Locate every Plasmodium falciparum-infected red blood cell.
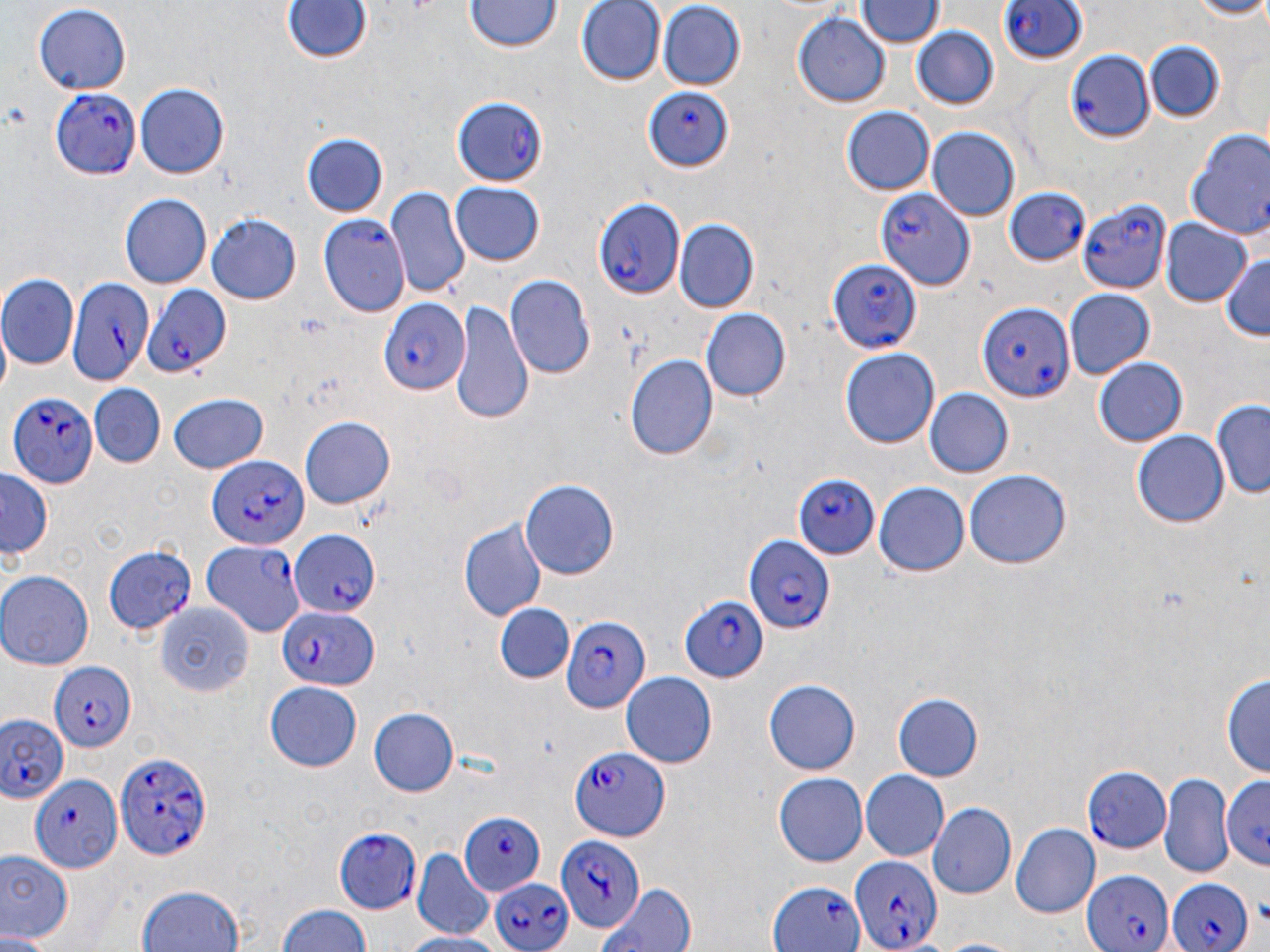

Approximate bounding boxes as named x1/y1/x2/y2 corners in pixels.
Plasmodium falciparum-infected red blood cells: (x1=994, y1=0, x2=1092, y2=75), (x1=1063, y1=48, x2=1151, y2=143), (x1=49, y1=86, x2=142, y2=179), (x1=644, y1=86, x2=734, y2=171), (x1=450, y1=96, x2=551, y2=184), (x1=874, y1=178, x2=977, y2=301), (x1=1003, y1=187, x2=1090, y2=273), (x1=593, y1=195, x2=687, y2=298), (x1=1077, y1=198, x2=1171, y2=295), (x1=319, y1=212, x2=411, y2=318), (x1=828, y1=259, x2=922, y2=353), (x1=65, y1=277, x2=149, y2=386), (x1=139, y1=282, x2=231, y2=378), (x1=378, y1=297, x2=469, y2=397), (x1=978, y1=299, x2=1075, y2=403), (x1=9, y1=393, x2=98, y2=490), (x1=208, y1=458, x2=307, y2=551), (x1=790, y1=475, x2=879, y2=560), (x1=289, y1=530, x2=381, y2=615), (x1=744, y1=534, x2=832, y2=634), (x1=202, y1=539, x2=304, y2=639), (x1=103, y1=547, x2=196, y2=637), (x1=677, y1=596, x2=769, y2=684), (x1=274, y1=608, x2=377, y2=691), (x1=560, y1=612, x2=654, y2=711), (x1=48, y1=663, x2=135, y2=752), (x1=0, y1=712, x2=70, y2=806), (x1=568, y1=744, x2=670, y2=841), (x1=115, y1=751, x2=211, y2=862), (x1=1084, y1=766, x2=1171, y2=854), (x1=28, y1=775, x2=120, y2=872), (x1=457, y1=811, x2=545, y2=896), (x1=334, y1=825, x2=423, y2=914), (x1=555, y1=835, x2=642, y2=934), (x1=848, y1=853, x2=942, y2=951), (x1=1081, y1=870, x2=1172, y2=952), (x1=488, y1=875, x2=574, y2=952), (x1=1164, y1=876, x2=1255, y2=952), (x1=769, y1=880, x2=864, y2=952).

Uninfected red blood cell locations: (x1=578, y1=0, x2=663, y2=85), (x1=860, y1=0, x2=939, y2=48), (x1=1182, y1=0, x2=1270, y2=19), (x1=282, y1=2, x2=370, y2=67), (x1=463, y1=2, x2=561, y2=55), (x1=658, y1=3, x2=746, y2=88), (x1=33, y1=5, x2=134, y2=95), (x1=792, y1=13, x2=891, y2=108), (x1=910, y1=26, x2=999, y2=110), (x1=1143, y1=40, x2=1224, y2=121), (x1=136, y1=86, x2=229, y2=178), (x1=841, y1=104, x2=934, y2=195), (x1=927, y1=126, x2=1021, y2=221), (x1=1184, y1=127, x2=1270, y2=241), (x1=302, y1=133, x2=389, y2=218), (x1=451, y1=183, x2=546, y2=266), (x1=385, y1=188, x2=469, y2=300), (x1=119, y1=194, x2=211, y2=289), (x1=206, y1=213, x2=302, y2=305), (x1=1159, y1=219, x2=1252, y2=308), (x1=676, y1=221, x2=757, y2=311), (x1=1219, y1=252, x2=1270, y2=341), (x1=504, y1=274, x2=595, y2=382), (x1=1, y1=275, x2=79, y2=367), (x1=1065, y1=289, x2=1154, y2=379), (x1=452, y1=302, x2=533, y2=422), (x1=702, y1=307, x2=790, y2=403), (x1=841, y1=348, x2=940, y2=448), (x1=626, y1=355, x2=718, y2=462), (x1=1093, y1=357, x2=1188, y2=447), (x1=89, y1=384, x2=165, y2=464), (x1=925, y1=389, x2=1011, y2=479), (x1=165, y1=393, x2=270, y2=472), (x1=1211, y1=400, x2=1270, y2=502), (x1=300, y1=418, x2=395, y2=509), (x1=1131, y1=430, x2=1228, y2=528), (x1=964, y1=470, x2=1071, y2=571), (x1=0, y1=471, x2=52, y2=561), (x1=521, y1=479, x2=620, y2=580), (x1=876, y1=479, x2=973, y2=575), (x1=458, y1=518, x2=546, y2=623), (x1=0, y1=571, x2=93, y2=670), (x1=152, y1=602, x2=255, y2=691), (x1=493, y1=603, x2=573, y2=684), (x1=620, y1=672, x2=718, y2=769), (x1=1222, y1=673, x2=1270, y2=783), (x1=764, y1=678, x2=862, y2=775), (x1=264, y1=683, x2=363, y2=771), (x1=893, y1=692, x2=983, y2=783), (x1=370, y1=705, x2=462, y2=797), (x1=861, y1=770, x2=949, y2=862), (x1=772, y1=773, x2=867, y2=867), (x1=1159, y1=773, x2=1231, y2=875), (x1=1224, y1=774, x2=1270, y2=872), (x1=927, y1=802, x2=1017, y2=898), (x1=1010, y1=823, x2=1100, y2=918), (x1=0, y1=847, x2=73, y2=947), (x1=411, y1=852, x2=493, y2=941), (x1=596, y1=881, x2=695, y2=952), (x1=135, y1=882, x2=246, y2=952), (x1=274, y1=901, x2=375, y2=952), (x1=399, y1=932, x2=511, y2=952), (x1=0, y1=933, x2=54, y2=952). Slide-level diagnosis: Plasmodium falciparum. Light microscopy. One field of a larger specimen. Image is 1270×952 pixels. Thin blood smear. May-Grünwald-Giemsa-stained preparation. 1000x magnification.